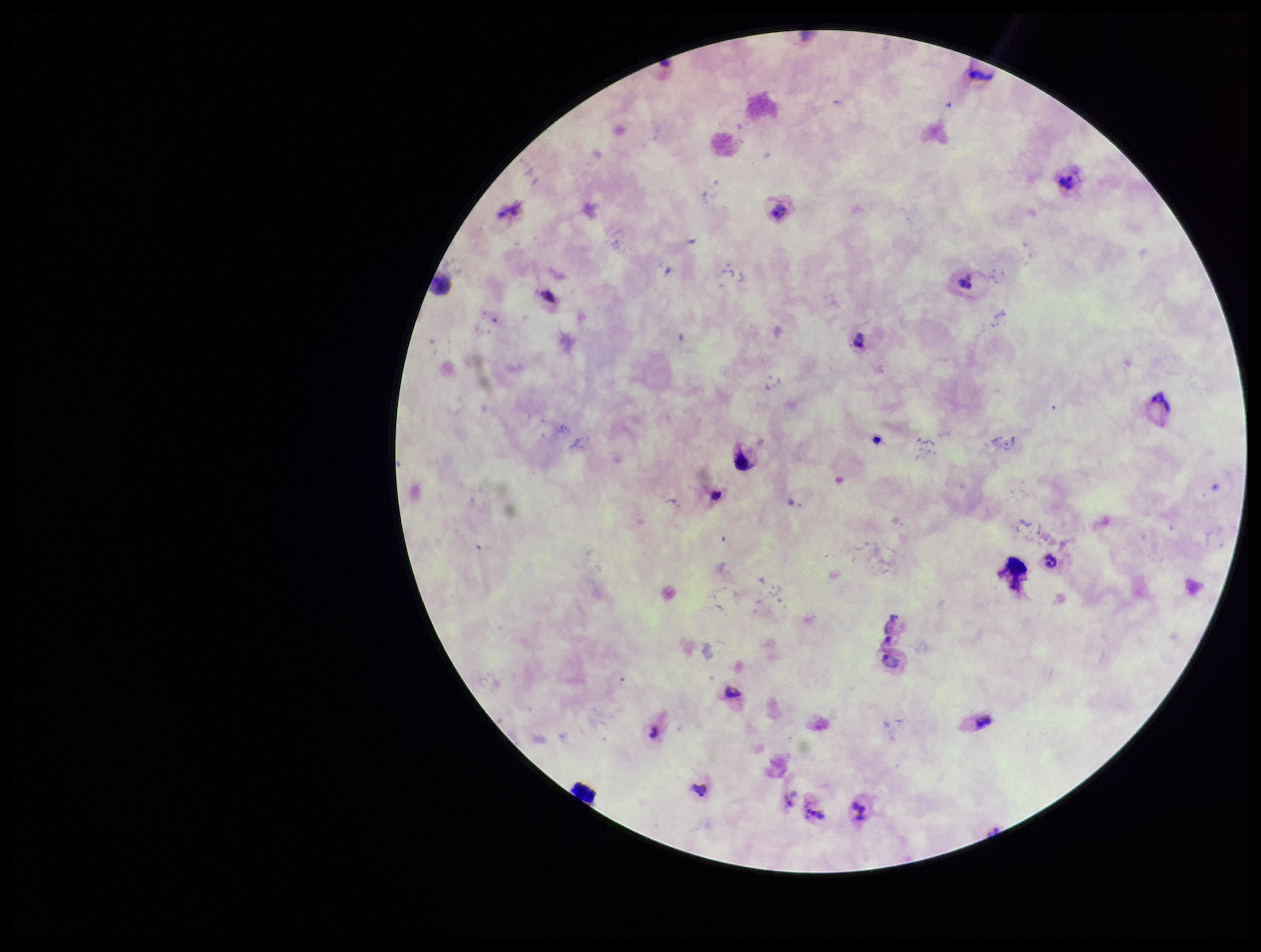

Summary:
  - Stain: Giemsa
  - Parasite count: 4
  - Field of view: single
  - Capture: smartphone photograph through the microscope eyepiece
  - Patient malaria status: positive
  - Preparation: thick blood smear
  - Leukocyte count: 1
  - Image size: 1261×952 pixels
  - Plasmodium parasites: seen
  - Species reported for this patient: Plasmodium vivax